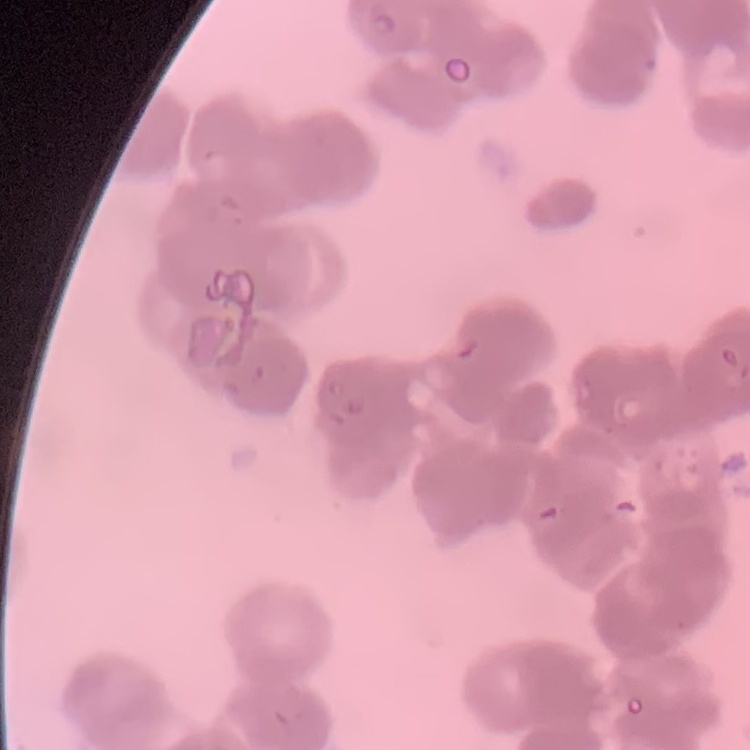

Summary:
  - Red blood cell morphology: rouleaux formation
  - Preparation: thin peripheral smear
  - Image type: one tile cut from a larger photomicrograph
  - Stain: Field's or Giemsa